Report the malaria status of this cell.
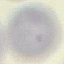
Uninfected.

{
  "preparation": "thin smear",
  "capture": "smartphone camera at the microscope eyepiece",
  "stain": "Giemsa",
  "image_type": "automatically extracted cell patch, resized to 64 × 64 pixels"
}